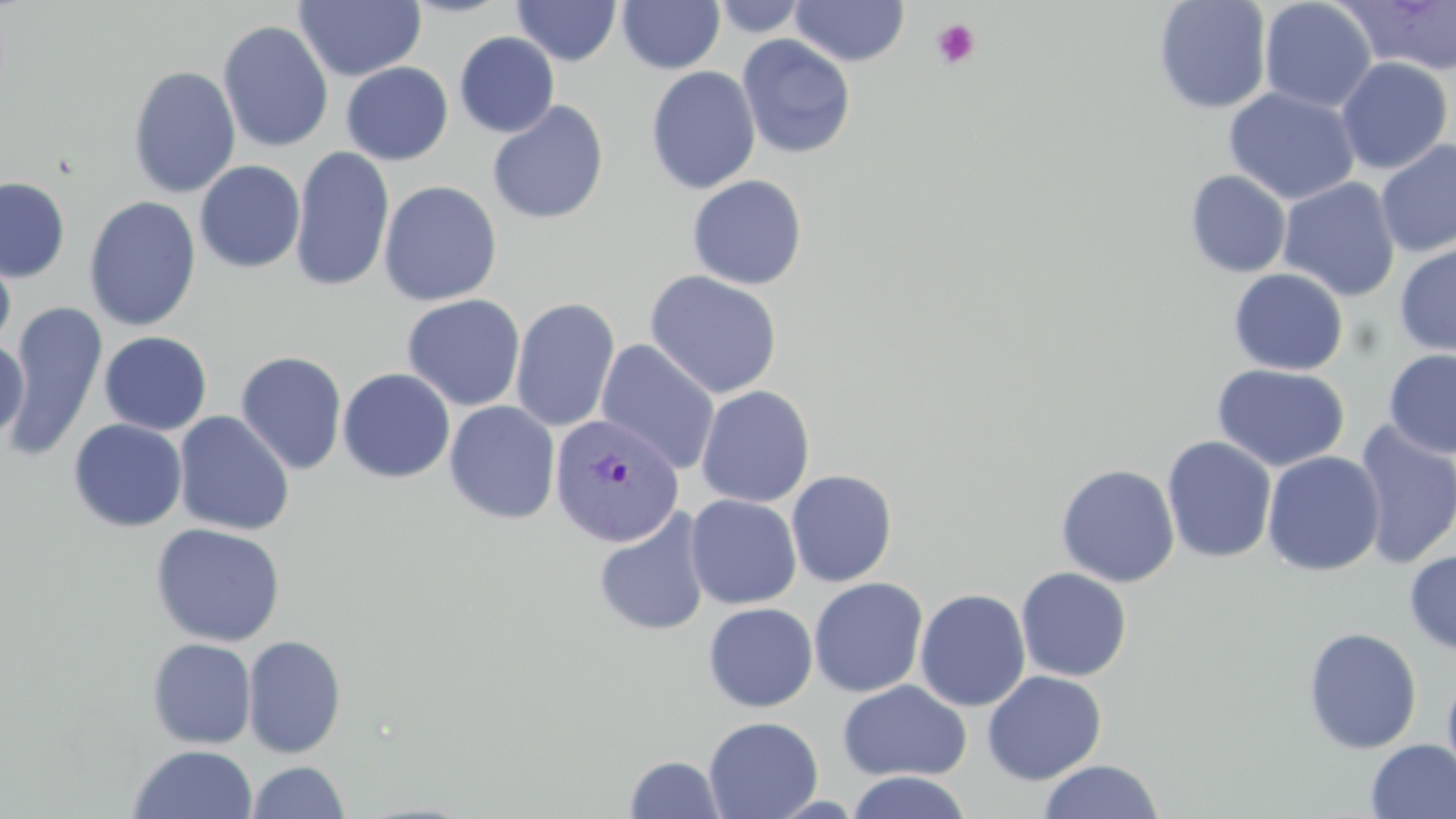

slide-level diagnosis = Plasmodium vivax
magnification = 1000x
modality = light microscopy
image size = 1456×819 pixels
Plasmodium vivax-infected red blood cell locations = approximate bounding boxes as (x1,y1)-(x2,y2) corner pairs in pixels: (549,413)-(685,548)
stain = May-Grünwald-Giemsa
uninfected red blood cell locations = approximate bounding boxes as (x1,y1)-(x2,y2) corner pairs in pixels: (711,0)-(811,38), (1153,0)-(1273,114), (1258,0)-(1377,114), (1339,0)-(1456,75), (293,1)-(426,82), (511,1)-(622,66), (617,1)-(725,74), (790,1)-(910,67), (217,19)-(334,153), (454,32)-(560,138), (736,34)-(856,160), (1335,57)-(1453,175), (341,61)-(454,165), (127,65)-(241,198), (645,66)-(761,195), (1223,87)-(1360,206), (486,99)-(609,225), (1375,139)-(1456,258), (290,146)-(395,293), (194,160)-(306,273), (1185,170)-(1291,278), (686,174)-(808,290), (0,176)-(71,282), (1277,177)-(1401,302), (119,180)-(250,317), (377,181)-(502,307), (83,196)-(201,331), (1393,241)-(1456,359), (0,242)-(16,352), (1228,268)-(1349,376), (644,270)-(783,399), (401,294)-(525,412), (510,297)-(620,432), (6,300)-(108,461), (99,331)-(213,435), (0,337)-(29,443), (595,340)-(720,475), (1383,349)-(1456,459), (235,350)-(348,475), (1211,363)-(1350,472), (337,368)-(456,484), (696,385)-(815,508), (444,401)-(560,524), (173,411)-(295,536), (68,418)-(188,532), (1351,420)-(1456,569), (1161,435)-(1277,564), (1262,451)-(1385,577), (1055,463)-(1180,588), (786,469)-(898,587), (685,494)-(802,610), (593,510)-(711,637), (149,522)-(286,647), (1404,548)-(1456,654), (1016,567)-(1133,682), (808,577)-(928,698), (914,588)-(1031,711), (702,602)-(818,713), (1302,626)-(1422,755), (242,634)-(347,758), (147,637)-(256,749), (982,670)-(1107,784), (1441,670)-(1456,791), (837,679)-(972,782), (703,716)-(823,819), (1365,739)-(1456,819), (128,744)-(258,819), (623,754)-(727,818), (1038,759)-(1164,818), (247,760)-(349,818), (845,771)-(973,819)
preparation = thin blood film
field of view = one of a larger specimen
platelet locations = approximate bounding boxes as (x1,y1)-(x2,y2) corner pairs in pixels: (930,18)-(981,70)